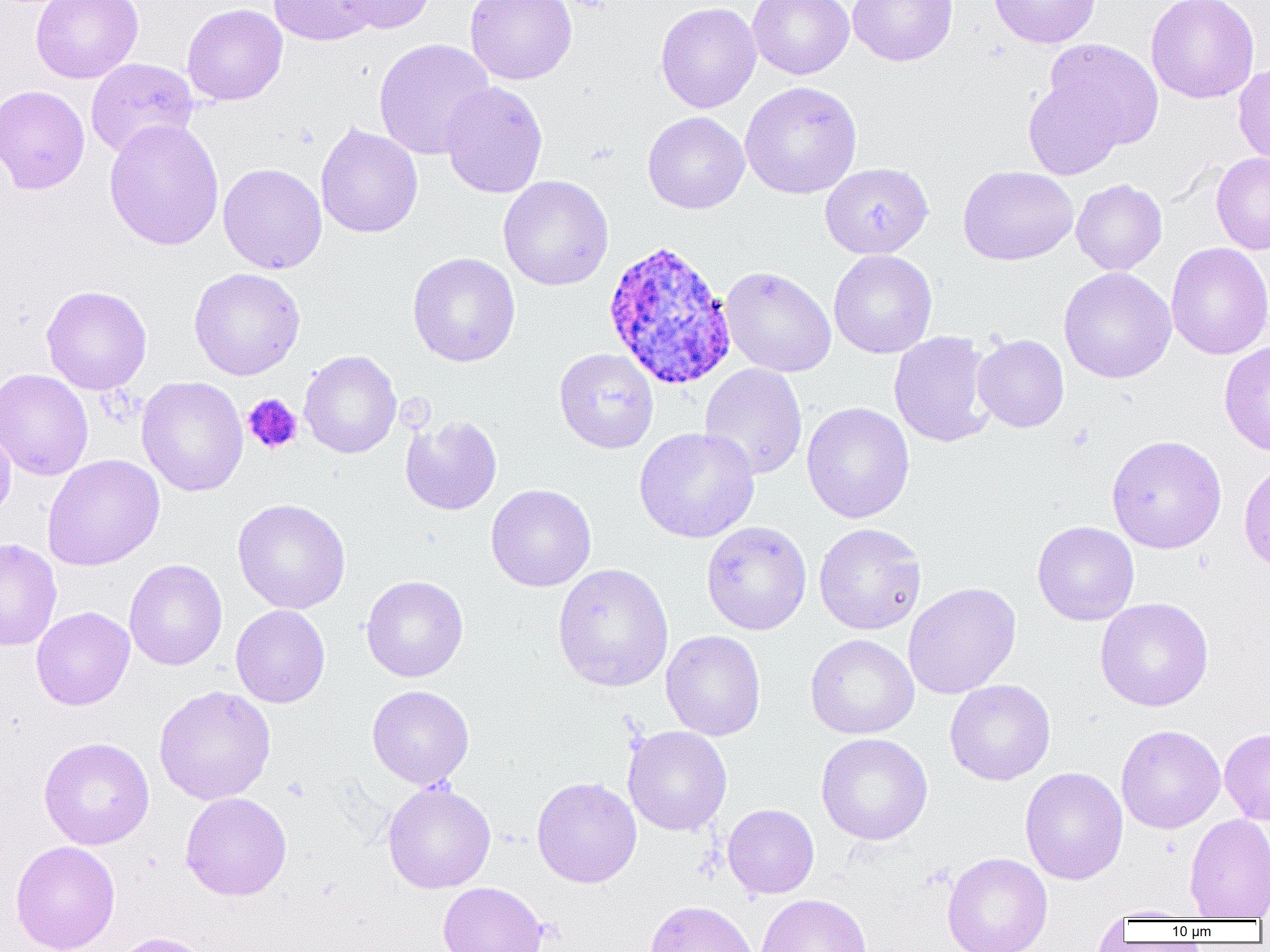
Approximate bounding boxes as (x1,y1)-(x2,y2) corner pairs in pixels. Uninfected red blood cell locations: (31,0)-(143,83), (268,0)-(378,46), (335,0)-(436,34), (465,0)-(577,85), (748,0)-(854,79), (847,0)-(957,66), (988,0)-(1101,49), (1146,0)-(1259,104), (655,1)-(761,113), (182,3)-(288,106), (373,38)-(495,160), (1044,38)-(1163,151), (85,58)-(198,158), (1233,63)-(1270,167), (1024,76)-(1126,180), (440,81)-(548,199), (740,81)-(862,199), (0,84)-(90,195), (642,111)-(749,214), (103,118)-(225,251), (315,122)-(423,239), (1211,152)-(1270,255), (820,162)-(933,259), (218,163)-(327,274), (958,165)-(1078,266), (498,175)-(613,291), (1071,179)-(1168,275), (1165,242)-(1270,360), (828,250)-(937,358), (407,252)-(521,367), (719,266)-(836,377), (188,267)-(305,380), (1058,267)-(1176,383), (41,285)-(152,395), (889,331)-(995,448), (973,334)-(1069,432), (1219,340)-(1270,457), (554,348)-(659,454), (299,350)-(402,459), (699,363)-(807,480), (0,368)-(93,481), (136,376)-(248,497), (801,401)-(915,524), (400,415)-(502,516), (0,419)-(16,522), (634,427)-(760,543), (1106,434)-(1227,554), (42,454)-(164,571), (1238,459)-(1270,574), (486,484)-(597,592), (232,498)-(351,614), (1032,520)-(1139,626), (701,521)-(812,635), (814,523)-(927,635), (0,538)-(62,651), (124,559)-(228,671), (552,562)-(674,693), (361,575)-(469,682), (902,582)-(1021,699), (1095,597)-(1214,712), (231,605)-(330,708), (31,606)-(135,710), (661,630)-(766,741), (805,633)-(919,739), (945,679)-(1055,785), (153,685)-(276,805), (367,685)-(474,789), (1116,724)-(1226,833), (623,725)-(732,836), (1220,728)-(1270,825), (816,733)-(933,845), (39,737)-(154,849), (1020,767)-(1128,885), (531,776)-(642,888), (382,781)-(496,894), (180,791)-(292,901), (722,804)-(819,899), (1184,813)-(1270,919), (10,840)-(121,952), (941,852)-(1053,952), (437,881)-(547,952), (755,893)-(872,952), (645,900)-(759,952), (1099,905)-(1201,922), (111,932)-(212,952). Plasmodium ovale-infected red blood cell locations: (602,239)-(738,391). Platelet locations: (563,0)-(612,12), (243,393)-(303,454). Slide-level diagnosis: Plasmodium ovale. Image is 1270×952 pixels. Single field of view. 1000x magnification. Optical microscopy. Thin blood film.